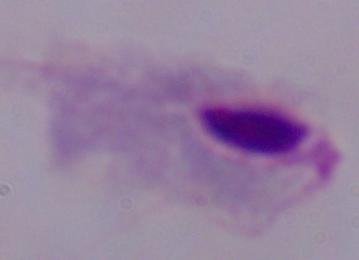
Summary:
  - Modality: photomicrograph
  - Identification: trichomonad
  - Magnification: 1000x